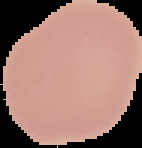

{
  "image_type": "cell region segmented out of the field of view; surrounding area masked to black",
  "result": "no malaria parasites seen",
  "preparation": "thin blood film",
  "image_size": "142×148 pixels"
}